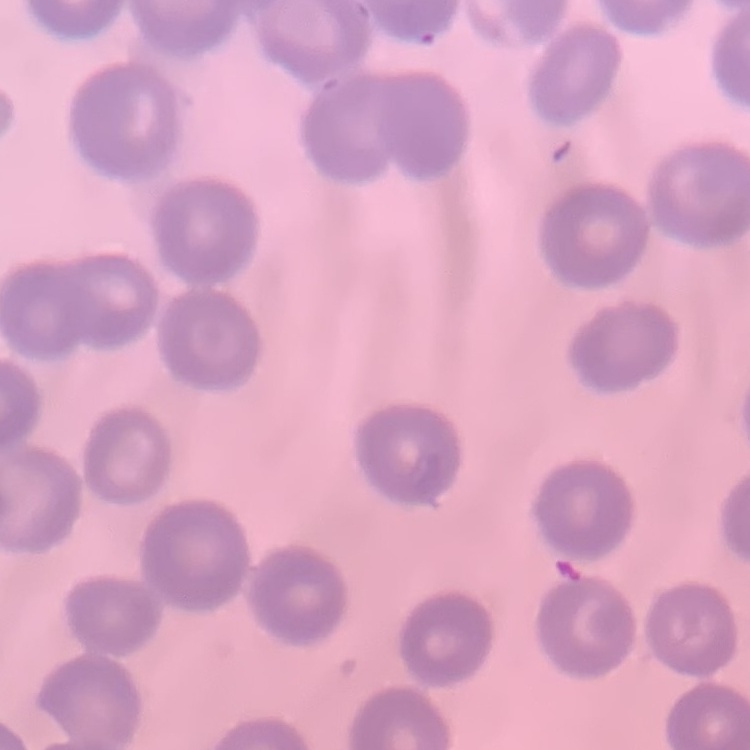

{
  "red_blood_cell_morphology": "no rouleaux formation",
  "preparation": "thin peripheral smear",
  "stain": "Field's or Giemsa",
  "image_type": "one tile cut from a larger photomicrograph"
}